Locate every Plasmodium falciparum-infected red blood cell.
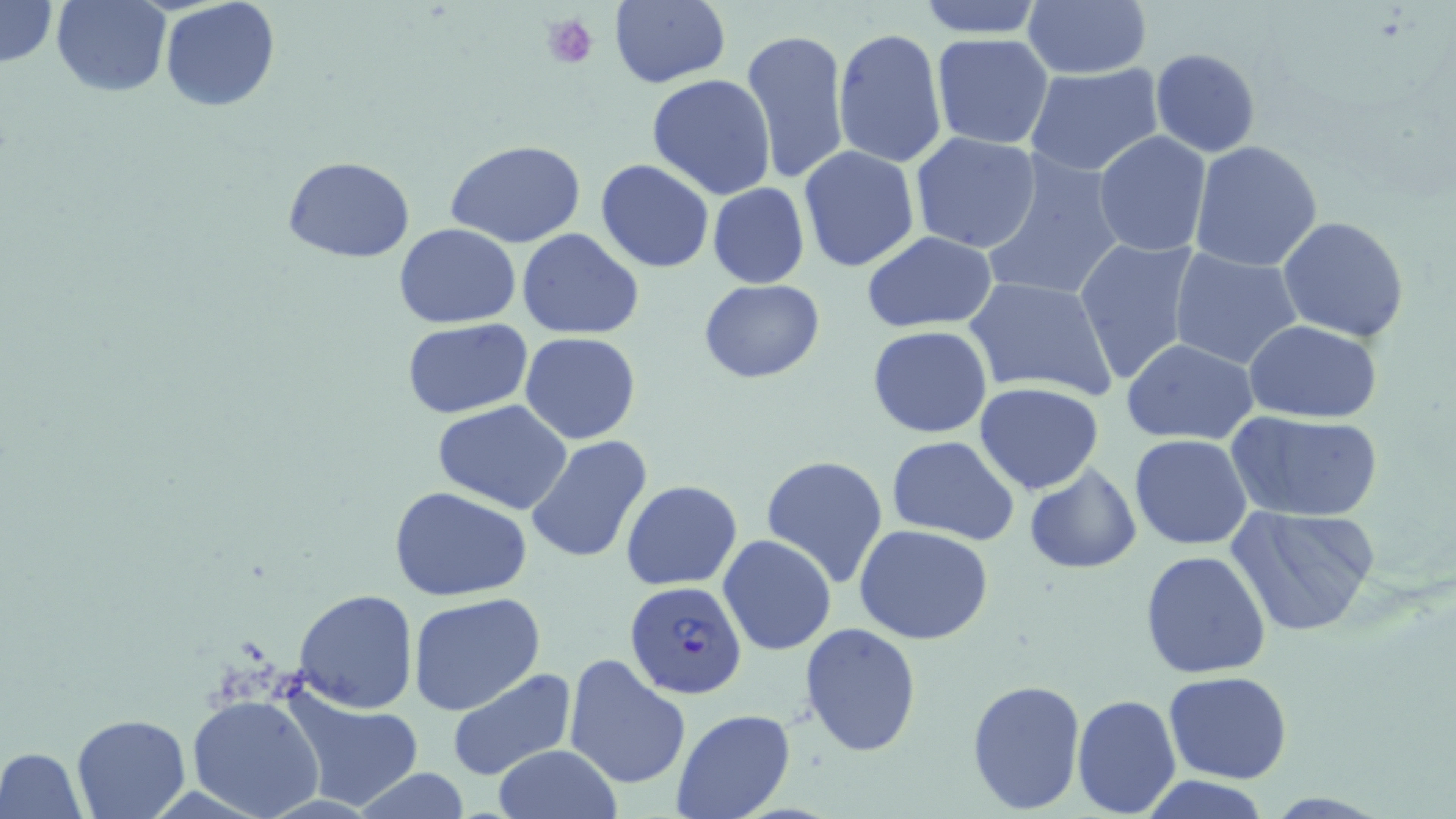
Approximate bounding boxes as (x1, y1, x2, y2) in pixels.
Plasmodium falciparum-infected red blood cells: (624, 580, 748, 701).

Summary:
  - Platelet locations: (541, 13, 597, 70)
  - Uninfected red blood cell locations: (0, 0, 58, 68), (52, 0, 170, 97), (160, 0, 280, 113), (917, 0, 1044, 39), (1022, 0, 1152, 79), (607, 1, 730, 88), (739, 28, 851, 185), (833, 28, 948, 169), (931, 34, 1055, 150), (1150, 48, 1260, 157), (1025, 63, 1165, 178), (647, 73, 777, 200), (1093, 130, 1213, 258), (909, 132, 1041, 255), (446, 140, 590, 249), (1190, 140, 1323, 271), (797, 145, 921, 273), (979, 152, 1125, 303), (282, 156, 416, 264), (595, 160, 714, 273), (707, 183, 810, 287), (1278, 216, 1409, 340), (394, 222, 522, 328), (517, 230, 644, 340), (862, 231, 997, 333), (1072, 236, 1201, 387), (1169, 248, 1306, 371), (963, 274, 1118, 402), (698, 279, 823, 384), (402, 319, 532, 417), (1245, 319, 1384, 422), (868, 326, 994, 439), (518, 332, 641, 444), (1121, 339, 1260, 444), (975, 382, 1106, 495), (432, 402, 573, 514), (1227, 411, 1385, 523), (527, 434, 654, 563), (1130, 434, 1253, 550), (886, 436, 1021, 546), (760, 455, 889, 586), (1024, 465, 1143, 574), (622, 480, 743, 589), (390, 487, 533, 601), (1229, 506, 1380, 637), (854, 526, 994, 646), (717, 534, 837, 657), (1140, 551, 1272, 680), (294, 589, 419, 712), (407, 594, 548, 718), (799, 623, 923, 758), (563, 654, 691, 788), (445, 668, 579, 784), (1163, 670, 1292, 784), (967, 678, 1087, 813), (284, 687, 425, 809), (187, 693, 326, 819), (1072, 693, 1182, 818), (671, 709, 797, 819), (71, 714, 192, 819), (493, 744, 620, 818), (0, 747, 88, 819), (348, 767, 475, 819), (1140, 776, 1273, 818)
  - Slide-level diagnosis: Plasmodium falciparum
  - Field of view: one of a larger specimen
  - Magnification: 1000x
  - Modality: optical microscopy
  - Stain: May-Grünwald-Giemsa
  - Preparation: thin blood film
  - Image size: 1456×819 pixels